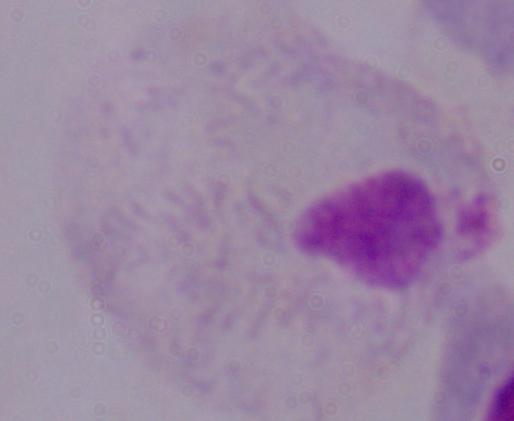
identification = trichomonad
modality = micrograph
magnification = 1000x